Report the malaria status of this cell.
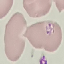

Uninfected.

Summary:
  - Stain: Giemsa
  - Preparation: thin blood film
  - Image type: cell patch, automatically extracted from a larger field of view and resized to 64 × 64 pixels
  - Capture: smartphone through the microscope eyepiece